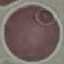

result = no malaria parasites detected
capture = smartphone camera at the microscope eyepiece
image type = automatically extracted cell patch, resized to 64 × 64 pixels
stain = Giemsa
preparation = thin blood smear